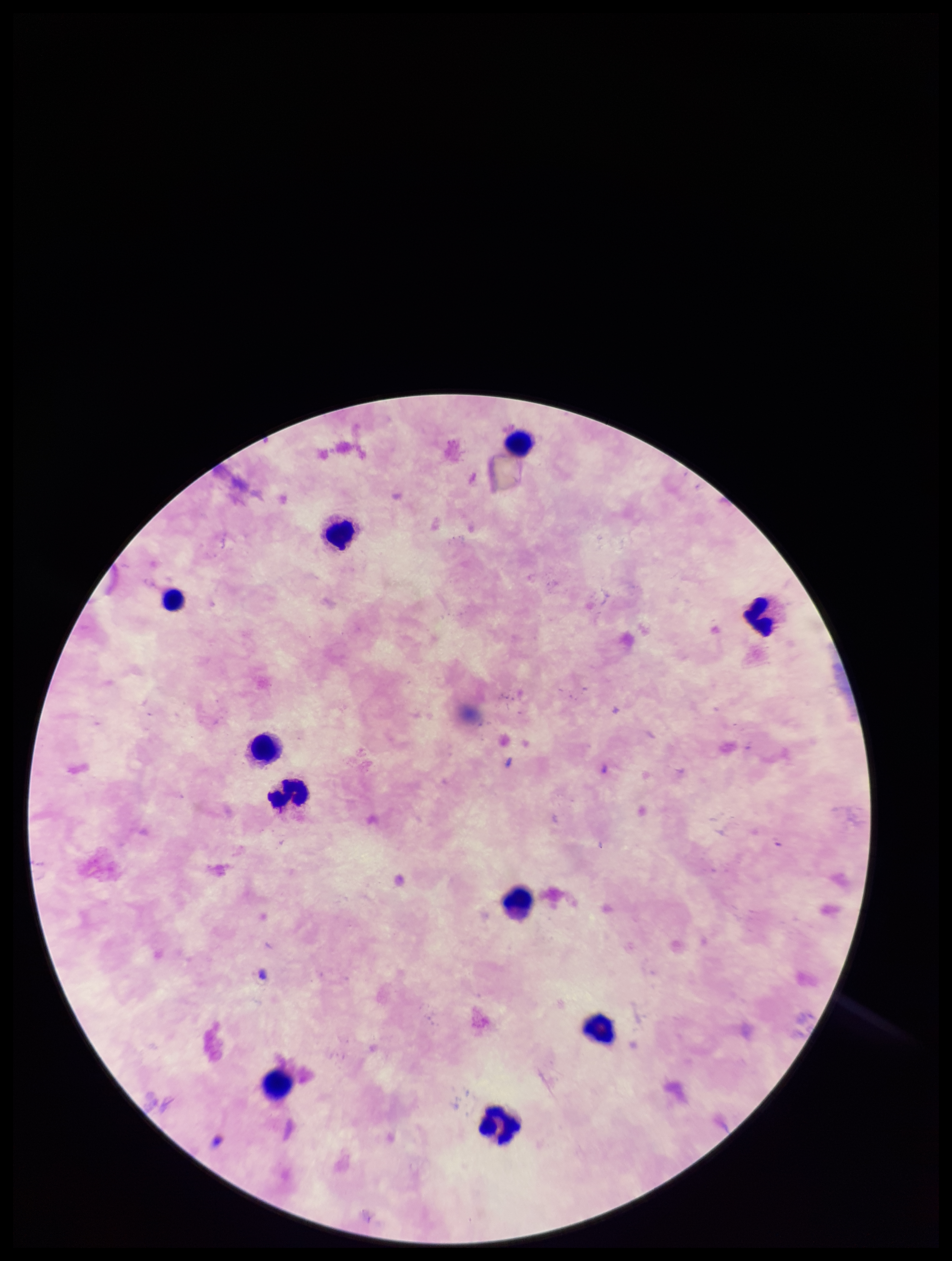
Summary:
  - Plasmodium parasites: none identified
  - Stain: Giemsa
  - Leukocyte count: 10
  - Species reported for this patient: Plasmodium falciparum
  - Image size: 952×1261 pixels
  - Patient malaria status: infected
  - Parasite count: 0
  - Preparation: thick
  - Capture: smartphone photograph through the microscope eyepiece
  - Field of view: one from this slide